State which parasite is depicted.
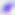

Toxoplasma gondii.

Micrograph. Captured at 400x magnification.